Assess this cell for malaria.
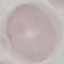

Uninfected.

Summary:
  - Capture: smartphone through the microscope eyepiece
  - Preparation: thin smear
  - Image type: automatically extracted cell patch, resized to 64 × 64 pixels
  - Stain: Giemsa